Assess the morphology of the erythrocytes.
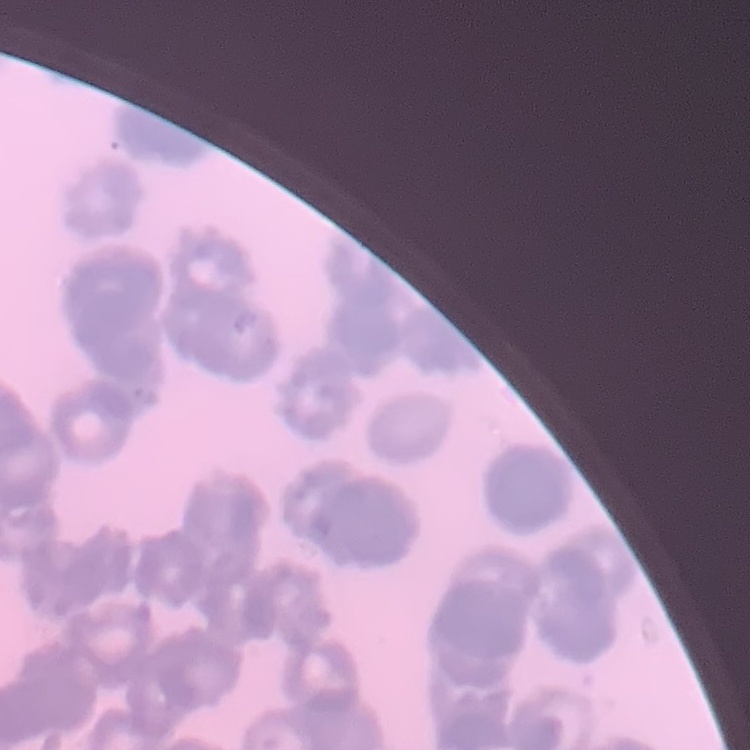
Rouleaux formation.

Thin blood smear. Stained with either Field's or Giemsa. Square crop of a larger photomicrograph.